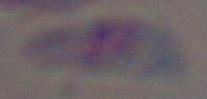
Summary:
  - Magnification: 1000x
  - Identification: Toxoplasma gondii
  - Modality: photomicrograph